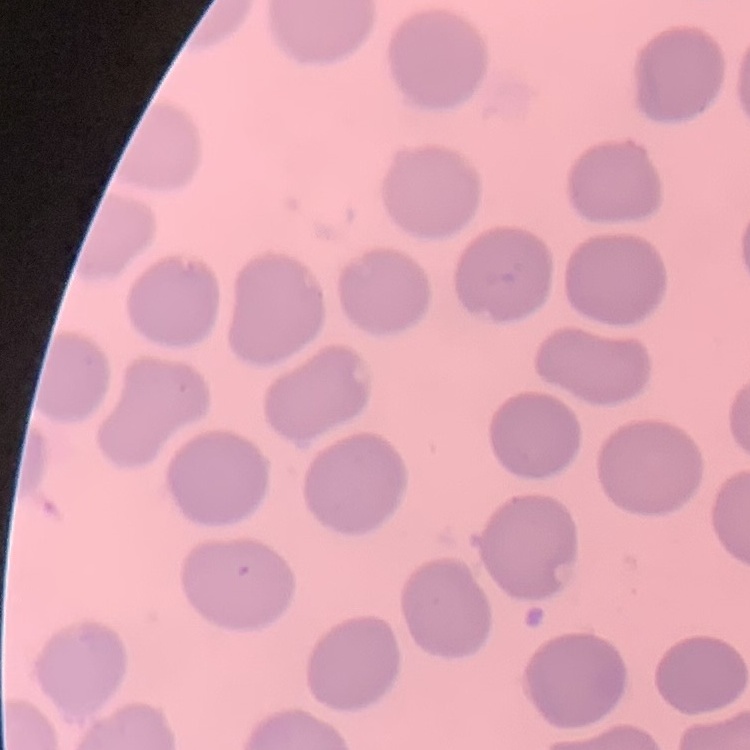 The red blood cells exhibit no rouleaux formation. One tile cut from a larger photomicrograph. Thin blood smear. Stained with either Field's or Giemsa.